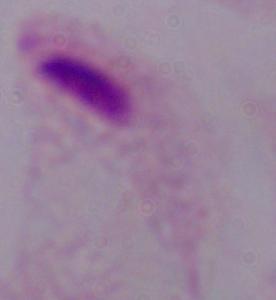
modality = micrograph
identification = trichomonad
magnification = 1000x